Comment on the morphology of the red blood cells.
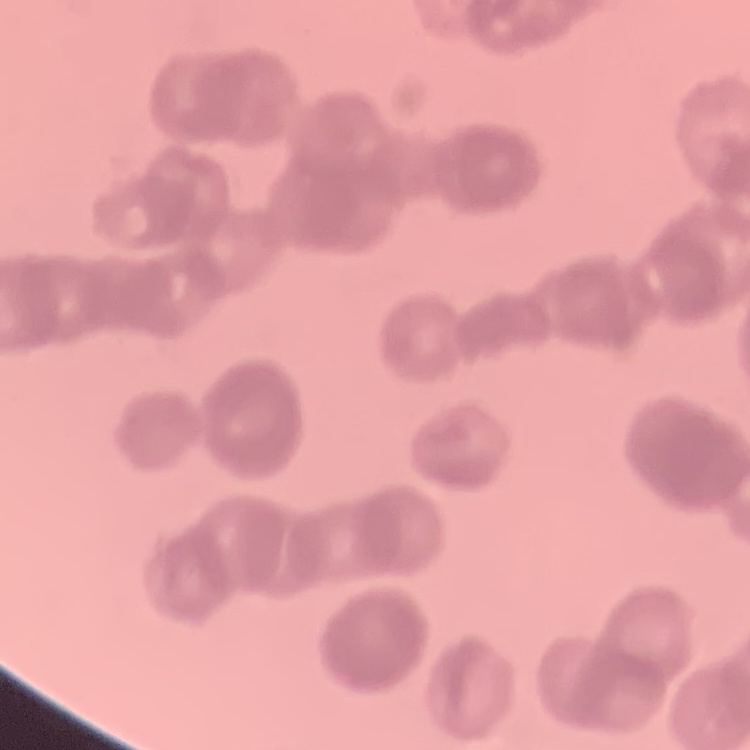
Rouleaux formation.

Square crop of a larger photomicrograph. Thin blood smear. Field's or Giemsa stain.